Outline platelets.
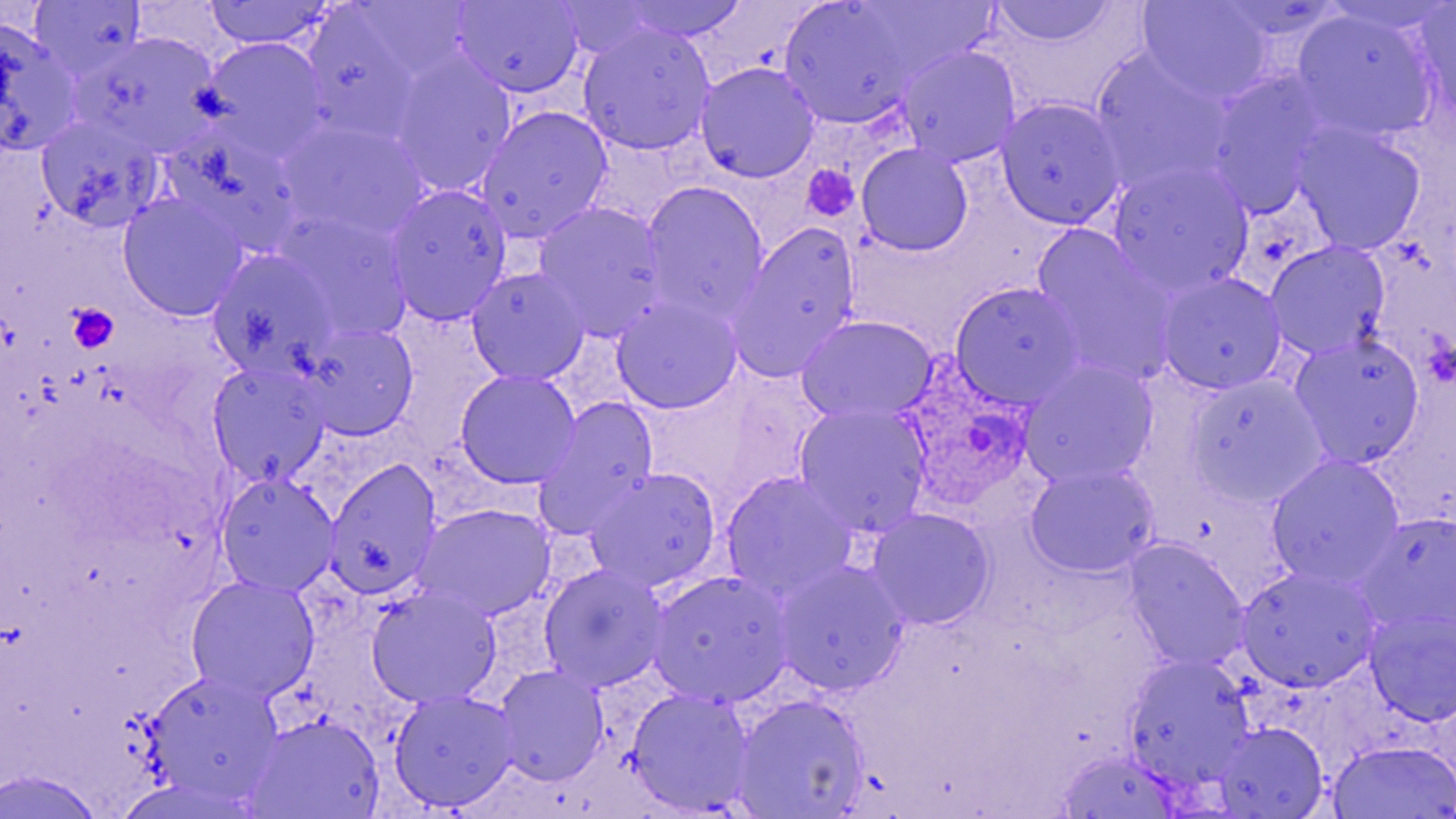
Approximate bounding boxes as named x1/y1/x2/y2 corners in pixels.
Platelets: (x1=801, y1=164, x2=860, y2=222), (x1=66, y1=303, x2=119, y2=354).

Plasmodium ovale-infected red blood cell locations: (x1=890, y1=359, x2=1041, y2=514). Uninfected red blood cell locations: (x1=31, y1=0, x2=146, y2=80), (x1=616, y1=0, x2=752, y2=43), (x1=989, y1=0, x2=1118, y2=47), (x1=1137, y1=0, x2=1274, y2=104), (x1=203, y1=1, x2=335, y2=50), (x1=451, y1=1, x2=585, y2=98), (x1=1412, y1=1, x2=1456, y2=124), (x1=779, y1=2, x2=919, y2=129), (x1=299, y1=6, x2=433, y2=144), (x1=1290, y1=7, x2=1440, y2=143), (x1=0, y1=19, x2=82, y2=156), (x1=578, y1=23, x2=715, y2=155), (x1=76, y1=33, x2=224, y2=158), (x1=200, y1=37, x2=330, y2=158), (x1=896, y1=45, x2=1021, y2=166), (x1=1091, y1=50, x2=1236, y2=196), (x1=388, y1=53, x2=517, y2=196), (x1=696, y1=62, x2=819, y2=182), (x1=1205, y1=73, x2=1328, y2=215), (x1=995, y1=98, x2=1125, y2=229), (x1=477, y1=107, x2=612, y2=240), (x1=35, y1=114, x2=163, y2=231), (x1=277, y1=121, x2=428, y2=245), (x1=1292, y1=124, x2=1426, y2=255), (x1=165, y1=126, x2=305, y2=256), (x1=856, y1=143, x2=974, y2=256), (x1=1107, y1=161, x2=1254, y2=298), (x1=641, y1=181, x2=768, y2=320), (x1=384, y1=184, x2=512, y2=325), (x1=118, y1=193, x2=248, y2=321), (x1=533, y1=202, x2=668, y2=339), (x1=272, y1=209, x2=414, y2=343), (x1=729, y1=223, x2=862, y2=381), (x1=1031, y1=229, x2=1174, y2=384), (x1=1265, y1=242, x2=1390, y2=360), (x1=205, y1=249, x2=339, y2=378), (x1=466, y1=267, x2=589, y2=385), (x1=1155, y1=271, x2=1287, y2=394), (x1=949, y1=281, x2=1085, y2=409), (x1=611, y1=296, x2=742, y2=414), (x1=797, y1=315, x2=937, y2=424), (x1=299, y1=324, x2=418, y2=439), (x1=1289, y1=334, x2=1424, y2=469), (x1=1018, y1=359, x2=1159, y2=488), (x1=207, y1=362, x2=331, y2=486), (x1=455, y1=370, x2=581, y2=488), (x1=1188, y1=374, x2=1326, y2=506), (x1=533, y1=398, x2=659, y2=535), (x1=794, y1=404, x2=930, y2=536), (x1=1266, y1=455, x2=1405, y2=589), (x1=324, y1=460, x2=441, y2=599), (x1=1024, y1=464, x2=1159, y2=578), (x1=586, y1=468, x2=721, y2=592), (x1=216, y1=473, x2=339, y2=596), (x1=721, y1=473, x2=856, y2=601), (x1=414, y1=504, x2=556, y2=620), (x1=866, y1=508, x2=994, y2=629), (x1=1358, y1=513, x2=1456, y2=636), (x1=1124, y1=540, x2=1249, y2=672), (x1=773, y1=561, x2=909, y2=696), (x1=539, y1=565, x2=669, y2=691), (x1=1237, y1=567, x2=1380, y2=693), (x1=648, y1=571, x2=794, y2=707), (x1=185, y1=575, x2=320, y2=702), (x1=366, y1=587, x2=502, y2=708), (x1=1365, y1=608, x2=1456, y2=725), (x1=1124, y1=655, x2=1255, y2=790), (x1=494, y1=665, x2=608, y2=786), (x1=145, y1=671, x2=283, y2=806), (x1=626, y1=689, x2=755, y2=814), (x1=388, y1=690, x2=520, y2=812), (x1=733, y1=695, x2=868, y2=818), (x1=244, y1=714, x2=384, y2=819), (x1=1211, y1=722, x2=1327, y2=818), (x1=1327, y1=740, x2=1456, y2=819), (x1=1056, y1=750, x2=1182, y2=818), (x1=0, y1=770, x2=106, y2=818). Slide-level diagnosis: Plasmodium ovale. Thin blood film. Image is 1456×819 pixels. Single field of view. Optical microscopy. 1000x magnification. May-Grünwald-Giemsa-stained preparation.